Assess this cell for malaria.
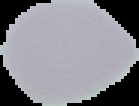
It is uninfected.

Image is 139×106 pixels. Segmented cell region on a black background. From a thin blood film.